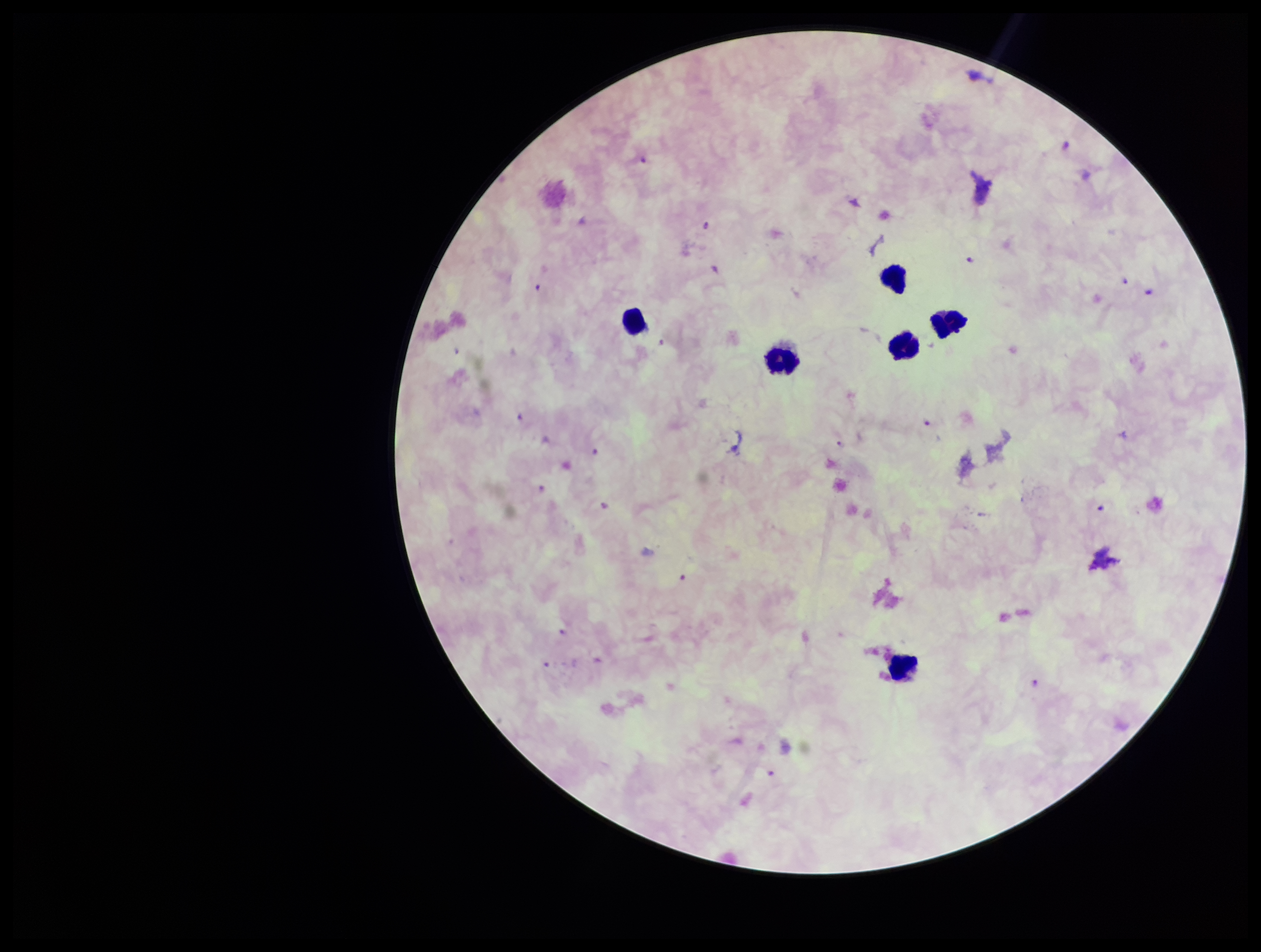
Patient malaria status: positive. Giemsa stain. Single field of view. Preparation: thick blood smear. Parasite count: 7. Plasmodium parasites: identified. Image is 1261×952 pixels. Photographed through the microscope eyepiece with a smartphone camera. Species reported for this patient: Plasmodium falciparum. Leukocyte count: 6.